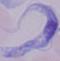
magnification = 1000x
modality = photomicrograph
identification = trypanosome